State the blood parasite species.
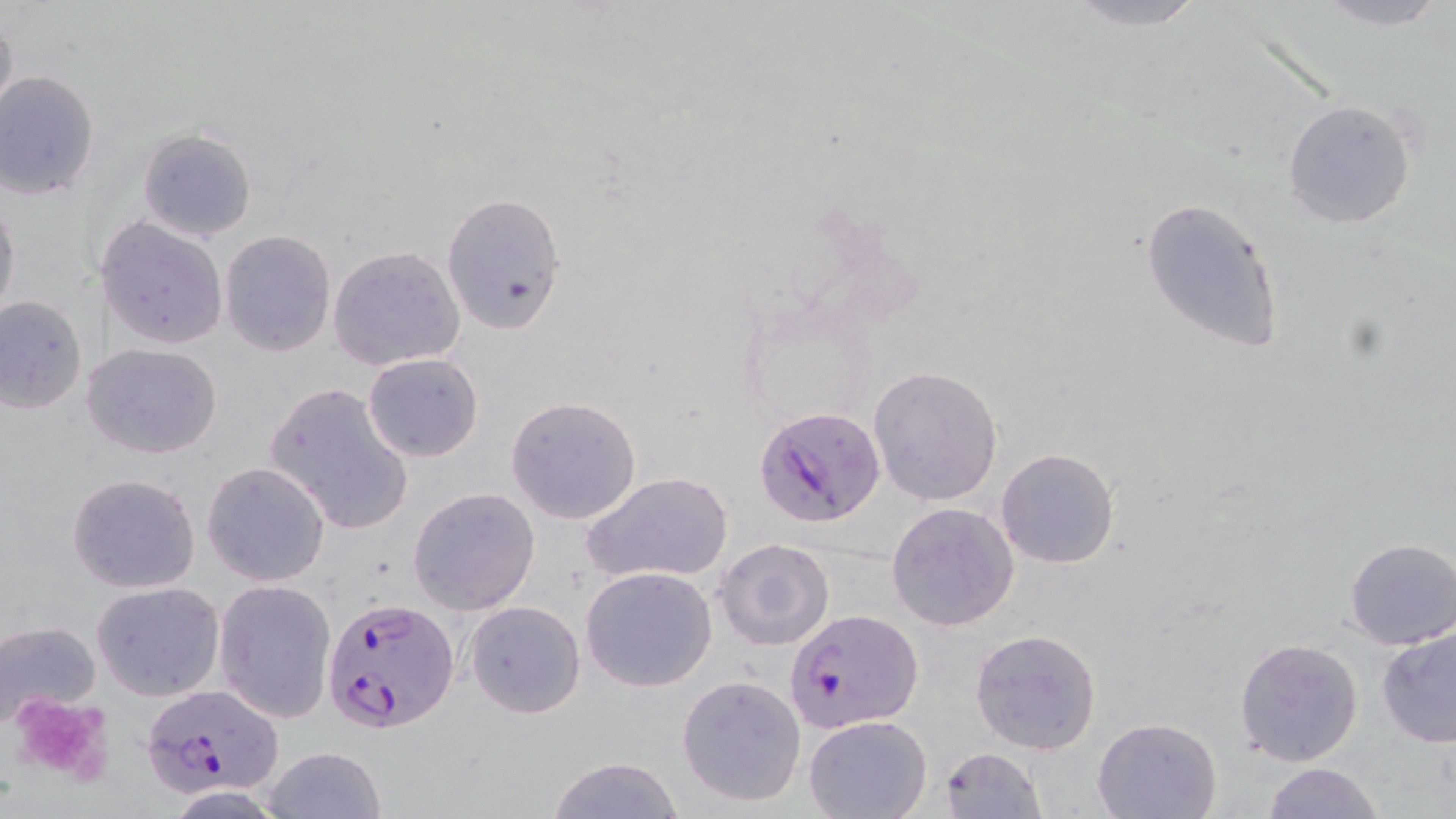
Plasmodium falciparum.

Summary:
  - Coordinate format: approximate bounding boxes as named x1/y1/x2/y2 corners in pixels
  - Uninfected red blood cell locations: (x1=1056, y1=0, x2=1212, y2=31), (x1=1306, y1=0, x2=1452, y2=30), (x1=0, y1=8, x2=18, y2=127), (x1=0, y1=72, x2=100, y2=200), (x1=1281, y1=98, x2=1419, y2=231), (x1=137, y1=127, x2=256, y2=241), (x1=441, y1=191, x2=566, y2=336), (x1=0, y1=194, x2=21, y2=326), (x1=1138, y1=194, x2=1286, y2=355), (x1=99, y1=216, x2=228, y2=351), (x1=219, y1=229, x2=337, y2=357), (x1=328, y1=245, x2=465, y2=372), (x1=0, y1=294, x2=87, y2=414), (x1=81, y1=342, x2=224, y2=459), (x1=363, y1=352, x2=483, y2=461), (x1=868, y1=365, x2=1004, y2=506), (x1=263, y1=381, x2=413, y2=535), (x1=505, y1=396, x2=641, y2=524), (x1=995, y1=448, x2=1122, y2=569), (x1=202, y1=461, x2=330, y2=587), (x1=585, y1=471, x2=734, y2=586), (x1=66, y1=473, x2=200, y2=594), (x1=408, y1=486, x2=540, y2=614), (x1=885, y1=501, x2=1019, y2=632), (x1=1344, y1=537, x2=1456, y2=650), (x1=715, y1=538, x2=834, y2=652), (x1=579, y1=566, x2=717, y2=692), (x1=216, y1=580, x2=337, y2=725), (x1=90, y1=581, x2=225, y2=702), (x1=463, y1=600, x2=585, y2=719), (x1=0, y1=618, x2=101, y2=725), (x1=1376, y1=626, x2=1456, y2=748), (x1=970, y1=627, x2=1102, y2=755), (x1=1233, y1=637, x2=1364, y2=767), (x1=676, y1=674, x2=806, y2=807), (x1=803, y1=715, x2=931, y2=819), (x1=1091, y1=716, x2=1222, y2=819), (x1=261, y1=745, x2=388, y2=819), (x1=937, y1=747, x2=1047, y2=819), (x1=547, y1=756, x2=683, y2=819), (x1=1262, y1=761, x2=1384, y2=819)
  - Platelet locations: (x1=7, y1=691, x2=117, y2=786)
  - Plasmodium falciparum-infected red blood cell locations: (x1=755, y1=406, x2=885, y2=529), (x1=323, y1=597, x2=459, y2=732), (x1=787, y1=609, x2=922, y2=731), (x1=140, y1=685, x2=283, y2=799)
  - Magnification: 1000x
  - Stain: May-Grünwald-Giemsa
  - Preparation: thin blood film
  - Modality: light microscopy
  - Image size: 1456×819 pixels
  - Field of view: single